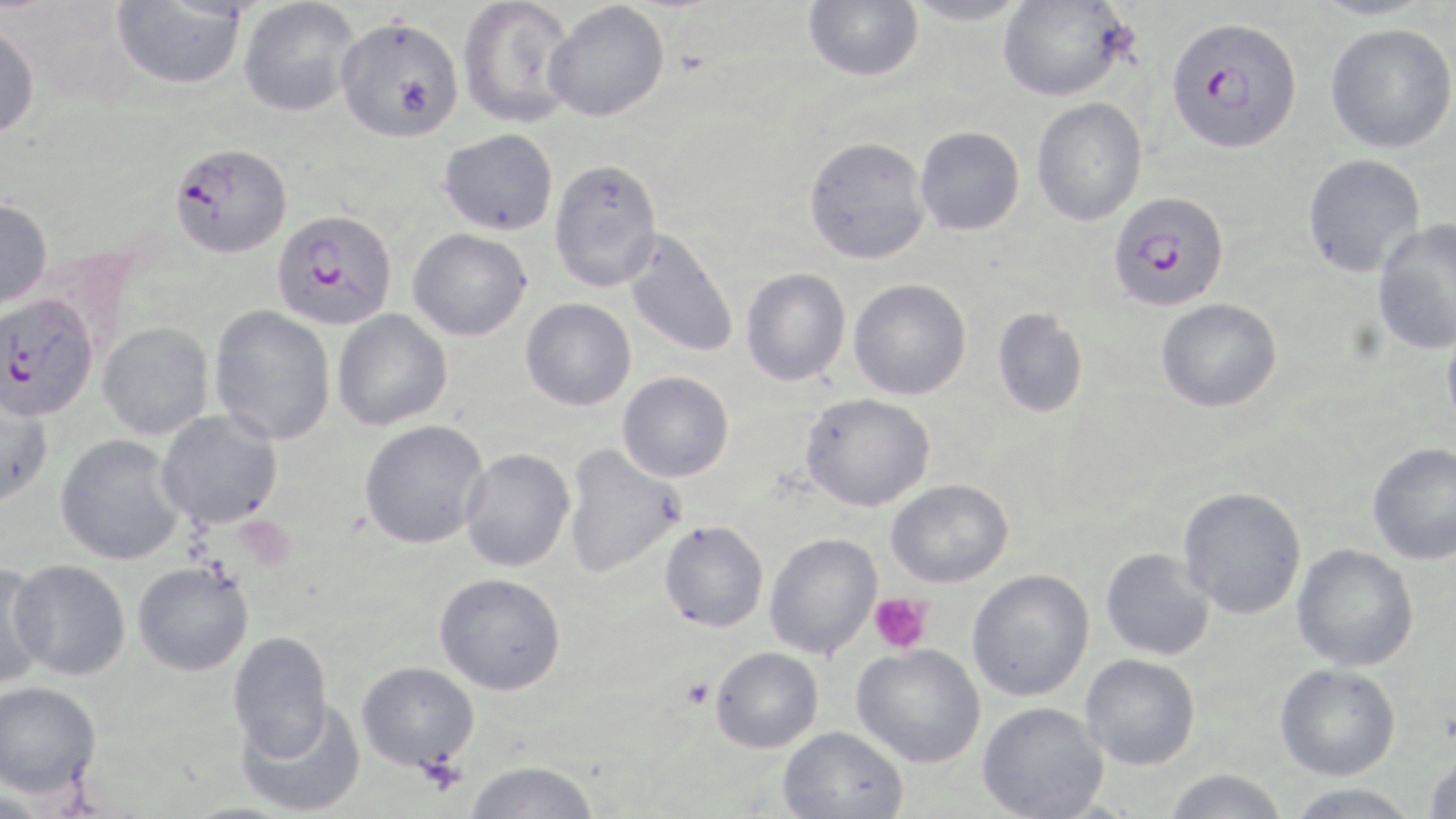
{
  "slide_level_diagnosis": "Plasmodium falciparum",
  "magnification": "1000x",
  "preparation": "thin blood film",
  "modality": "optical microscopy",
  "stain": "May-Grünwald-Giemsa",
  "uninfected_red_blood_cell_locations": "approximate bounding boxes as [x1, y1, x2, y2] in pixels: [458, 0, 579, 128], [803, 0, 923, 82], [903, 0, 1030, 26], [997, 0, 1131, 102], [1309, 0, 1436, 21], [112, 1, 246, 90], [238, 1, 361, 117], [544, 1, 669, 122], [335, 15, 464, 142], [0, 22, 41, 140], [1325, 23, 1456, 154], [1031, 98, 1147, 226], [915, 126, 1024, 235], [439, 128, 558, 236], [804, 136, 930, 265], [1302, 154, 1426, 278], [549, 157, 663, 291], [0, 197, 53, 312], [1371, 218, 1456, 355], [408, 228, 532, 341], [623, 229, 739, 358], [741, 268, 851, 386], [849, 279, 971, 400], [520, 298, 637, 411], [1156, 298, 1282, 413], [209, 306, 336, 446], [993, 308, 1088, 417], [332, 309, 452, 431], [1441, 320, 1456, 438], [98, 322, 214, 440], [618, 371, 734, 482], [0, 390, 53, 508], [800, 393, 935, 512], [157, 409, 284, 529], [359, 420, 491, 550], [55, 435, 186, 565], [1367, 442, 1456, 565], [562, 445, 686, 578], [460, 448, 575, 572], [886, 479, 1013, 588], [1178, 487, 1306, 620], [659, 520, 769, 632], [764, 532, 882, 659], [1292, 544, 1419, 672], [1100, 548, 1215, 661], [0, 559, 54, 689], [9, 559, 130, 680], [132, 561, 253, 676], [966, 569, 1094, 701], [435, 572, 566, 695], [227, 631, 334, 758], [851, 644, 985, 768], [710, 646, 824, 753], [1079, 654, 1200, 770], [356, 661, 479, 772], [1274, 663, 1401, 781], [0, 681, 101, 797], [238, 700, 366, 817], [976, 702, 1108, 819], [778, 725, 908, 818], [1424, 748, 1456, 818], [463, 760, 600, 819], [1164, 769, 1287, 819], [1284, 784, 1420, 818], [0, 790, 54, 819]",
  "plasmodium_falciparum_infected_red_blood_cell_locations": "approximate bounding boxes as [x1, y1, x2, y2] in pixels: [1168, 17, 1301, 154], [169, 141, 292, 259], [1108, 191, 1229, 312], [272, 208, 397, 330], [0, 293, 98, 421]",
  "platelet_locations": "approximate bounding boxes as [x1, y1, x2, y2] in pixels: [868, 592, 932, 654], [682, 678, 713, 709], [416, 755, 467, 795]",
  "field_of_view": "one of a larger specimen",
  "image_size": "1456×819 pixels"
}